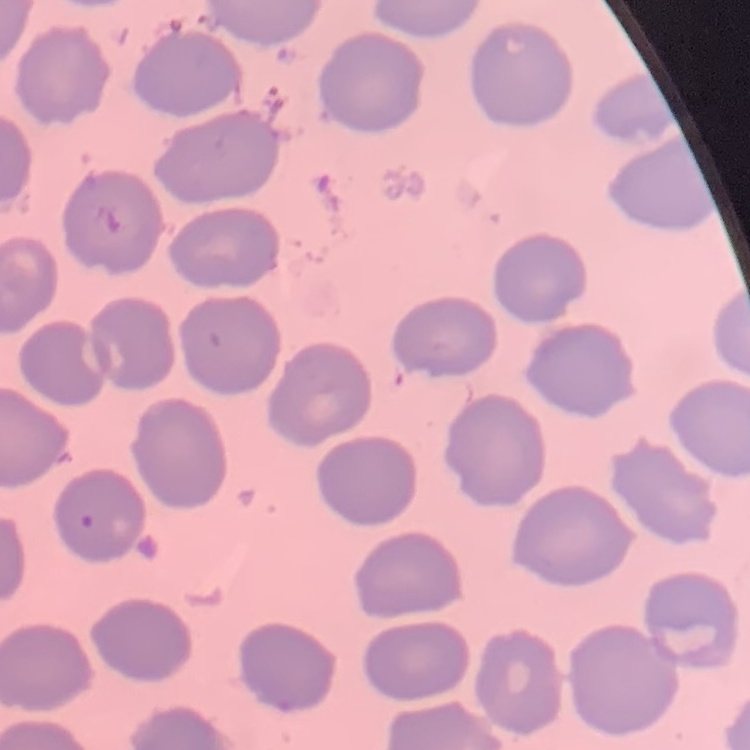
erythrocyte morphology = no rouleaux formation
stain = Field's or Giemsa
preparation = thin blood film
image type = one tile cut from a larger photomicrograph